Identify the parasite.
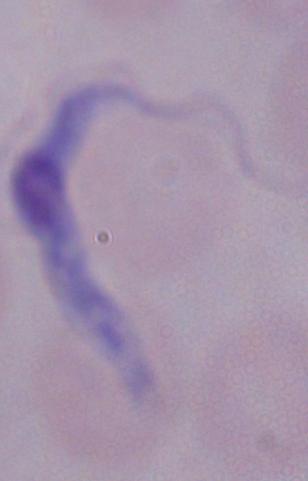
This is a trypanosome.

1000x magnification. Micrograph.